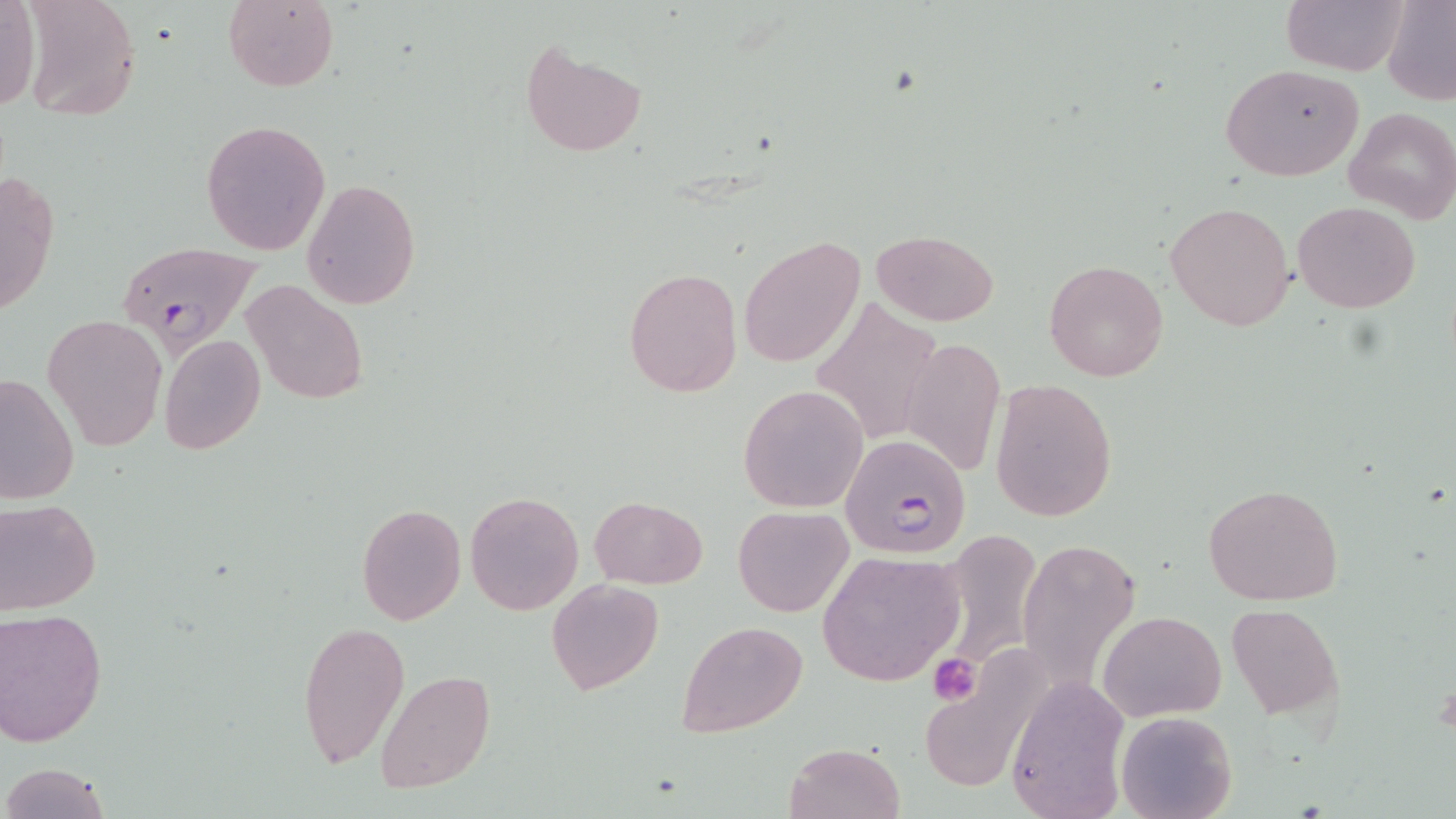

Approximate bounding boxes as (x1,y1)-(x2,y2) corner pairs in pixels. Uninfected red blood cell locations: (19,0)-(142,122), (223,0)-(339,92), (1279,0)-(1409,75), (1381,0)-(1456,106), (0,2)-(42,112), (520,42)-(646,159), (1220,63)-(1365,181), (1343,106)-(1456,224), (201,118)-(332,255), (2,165)-(61,322), (301,178)-(421,310), (1293,200)-(1420,312), (1165,201)-(1295,331), (870,229)-(997,325), (740,236)-(864,367), (1044,258)-(1169,382), (623,268)-(742,395), (240,278)-(369,406), (812,298)-(943,445), (44,314)-(166,451), (160,334)-(265,455), (901,334)-(1006,480), (0,370)-(78,506), (990,378)-(1116,524), (740,386)-(866,511), (1203,483)-(1346,607), (465,491)-(582,615), (590,496)-(707,587), (0,498)-(101,614), (357,504)-(466,623), (733,506)-(853,616), (1017,537)-(1141,690), (941,541)-(1039,686), (817,549)-(967,688), (547,577)-(664,695), (1226,604)-(1343,717), (0,606)-(109,746), (1098,609)-(1226,722), (296,620)-(409,768), (679,620)-(805,738), (920,666)-(1043,793), (376,670)-(493,796), (1003,677)-(1131,818), (1116,709)-(1236,819), (784,742)-(905,819), (2,762)-(110,819). Platelet locations: (926,653)-(981,707). Plasmodium falciparum-infected red blood cell locations: (114,242)-(264,355), (838,432)-(972,558). Slide-level diagnosis: Plasmodium falciparum. Single field of view. Thin blood smear. Image is 1456×819 pixels. 1000x magnification. Optical microscopy. May-Grünwald-Giemsa-stained preparation.